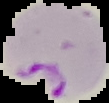
malaria_status: parasitized
preparation: thin blood film
image_type: segmented cell region on a black background
image_size: 109×103 pixels